Describe the morphology of the red blood cells.
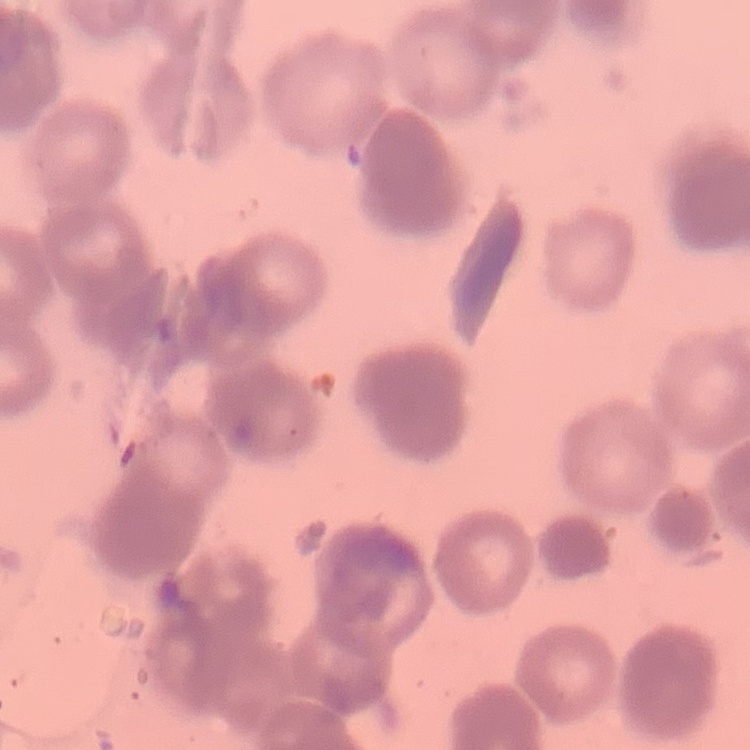

They show rouleaux formation.

Stained with either Field's or Giemsa. Square crop of a larger photomicrograph. Thin blood film.